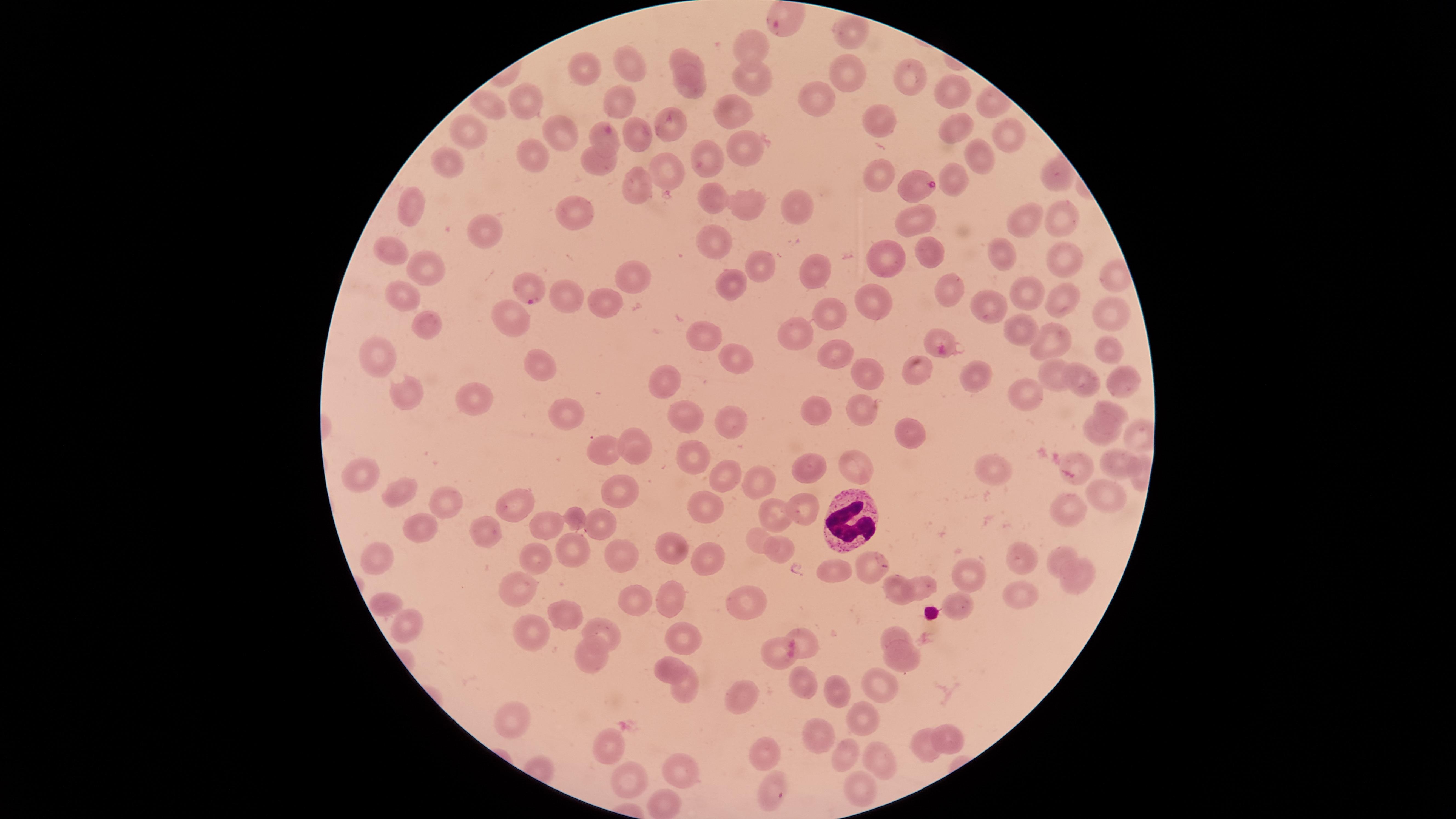

Approximate marker points, in pixels from the top-left corner. Parasitized red blood cells: (x=781, y=22), (x=917, y=186), (x=530, y=291). Uninfected red blood cells: (x=850, y=27), (x=750, y=44), (x=683, y=52), (x=625, y=60), (x=582, y=70), (x=843, y=70), (x=754, y=79), (x=916, y=80), (x=692, y=84), (x=951, y=93), (x=529, y=94), (x=813, y=97), (x=491, y=104), (x=617, y=106), (x=741, y=110), (x=884, y=122), (x=668, y=126), (x=637, y=129), (x=1000, y=129), (x=960, y=130), (x=554, y=131), (x=471, y=134), (x=607, y=139), (x=742, y=146), (x=536, y=154), (x=975, y=154), (x=706, y=156), (x=446, y=157), (x=604, y=164), (x=881, y=172), (x=663, y=176), (x=1052, y=177), (x=961, y=179), (x=634, y=192), (x=706, y=195), (x=748, y=206), (x=800, y=206), (x=414, y=208), (x=912, y=218), (x=1054, y=220), (x=578, y=221), (x=1019, y=223), (x=485, y=231), (x=712, y=237), (x=927, y=248), (x=389, y=250), (x=1003, y=251), (x=893, y=254), (x=1063, y=257), (x=423, y=262), (x=755, y=263), (x=814, y=264), (x=630, y=273), (x=733, y=284), (x=949, y=285), (x=1029, y=292), (x=1056, y=294), (x=402, y=296), (x=880, y=298), (x=571, y=299), (x=599, y=299), (x=994, y=305), (x=1112, y=306), (x=509, y=313), (x=828, y=315), (x=426, y=322), (x=799, y=327), (x=1017, y=333), (x=941, y=336), (x=709, y=338), (x=1047, y=339), (x=1107, y=346), (x=835, y=354), (x=374, y=356), (x=545, y=362), (x=747, y=364), (x=866, y=368), (x=922, y=370), (x=974, y=371), (x=661, y=375), (x=1054, y=375), (x=1118, y=379), (x=1087, y=381), (x=410, y=390), (x=478, y=397), (x=1026, y=397), (x=863, y=407), (x=564, y=409), (x=818, y=410), (x=1108, y=410), (x=729, y=419), (x=689, y=420), (x=903, y=429), (x=1098, y=434), (x=644, y=446), (x=609, y=449), (x=689, y=450), (x=1076, y=458), (x=1114, y=461), (x=354, y=463), (x=856, y=467), (x=725, y=469), (x=804, y=470), (x=995, y=473), (x=763, y=483), (x=405, y=492), (x=1098, y=493), (x=624, y=494), (x=441, y=500), (x=704, y=501), (x=506, y=504), (x=799, y=506), (x=768, y=509), (x=578, y=510), (x=1069, y=512), (x=600, y=518), (x=547, y=522), (x=425, y=528), (x=483, y=533), (x=758, y=535), (x=672, y=543), (x=1060, y=548), (x=380, y=550), (x=780, y=550), (x=576, y=552), (x=624, y=552), (x=1026, y=554), (x=704, y=556), (x=534, y=558), (x=874, y=560), (x=837, y=567), (x=967, y=572), (x=1080, y=574), (x=930, y=581), (x=520, y=588), (x=900, y=588), (x=1020, y=590), (x=630, y=594), (x=379, y=600), (x=674, y=601), (x=751, y=603), (x=957, y=603), (x=562, y=612), (x=603, y=627), (x=409, y=628), (x=898, y=631), (x=686, y=633), (x=803, y=635), (x=540, y=636), (x=588, y=657), (x=777, y=658), (x=901, y=659), (x=667, y=662), (x=877, y=680), (x=807, y=684), (x=683, y=689), (x=836, y=689), (x=743, y=699), (x=865, y=717), (x=509, y=720), (x=947, y=734), (x=824, y=738), (x=607, y=744), (x=922, y=749), (x=764, y=750), (x=845, y=751), (x=883, y=762), (x=684, y=768), (x=630, y=773), (x=771, y=793), (x=851, y=795), (x=664, y=805). White blood cells: (x=851, y=517). Giemsa stain. Thin smear of blood. Single field of view. Presence: malaria parasites identified. Image is 1456×819 pixels. Species: Plasmodium falciparum. Photographed with a smartphone camera through the microscope eyepiece. Circular visible region.